Describe the morphology of the red blood cells.
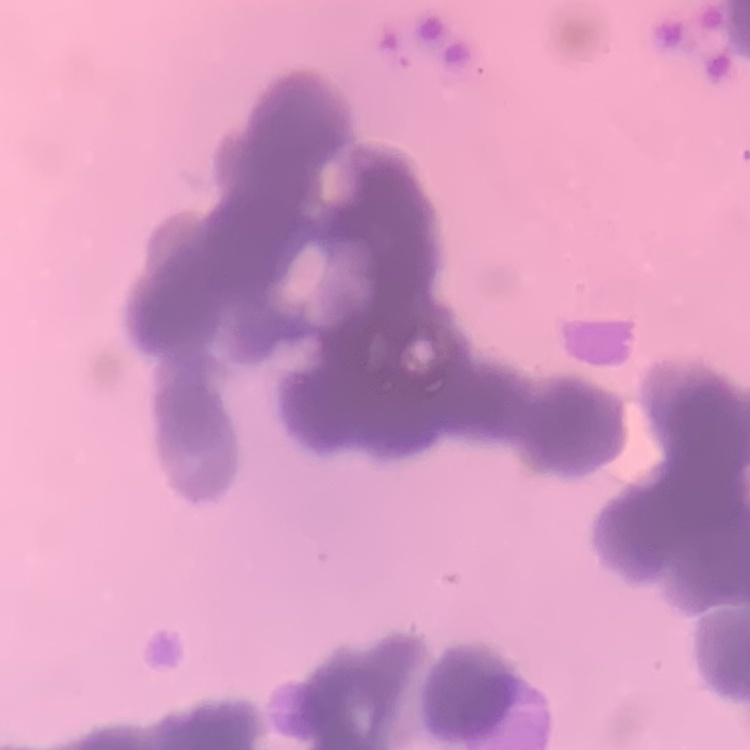

Rouleaux formation.

stain = Field's or Giemsa
image type = one tile cut from a larger photomicrograph
preparation = thin blood film